Assess this cell for malaria.
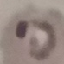
Parasitized.

Acquired by smartphone through the microscope eyepiece. Thin smear of blood. Giemsa stain. Cell patch, automatically extracted from a larger field of view and resized to 64 × 64 pixels.